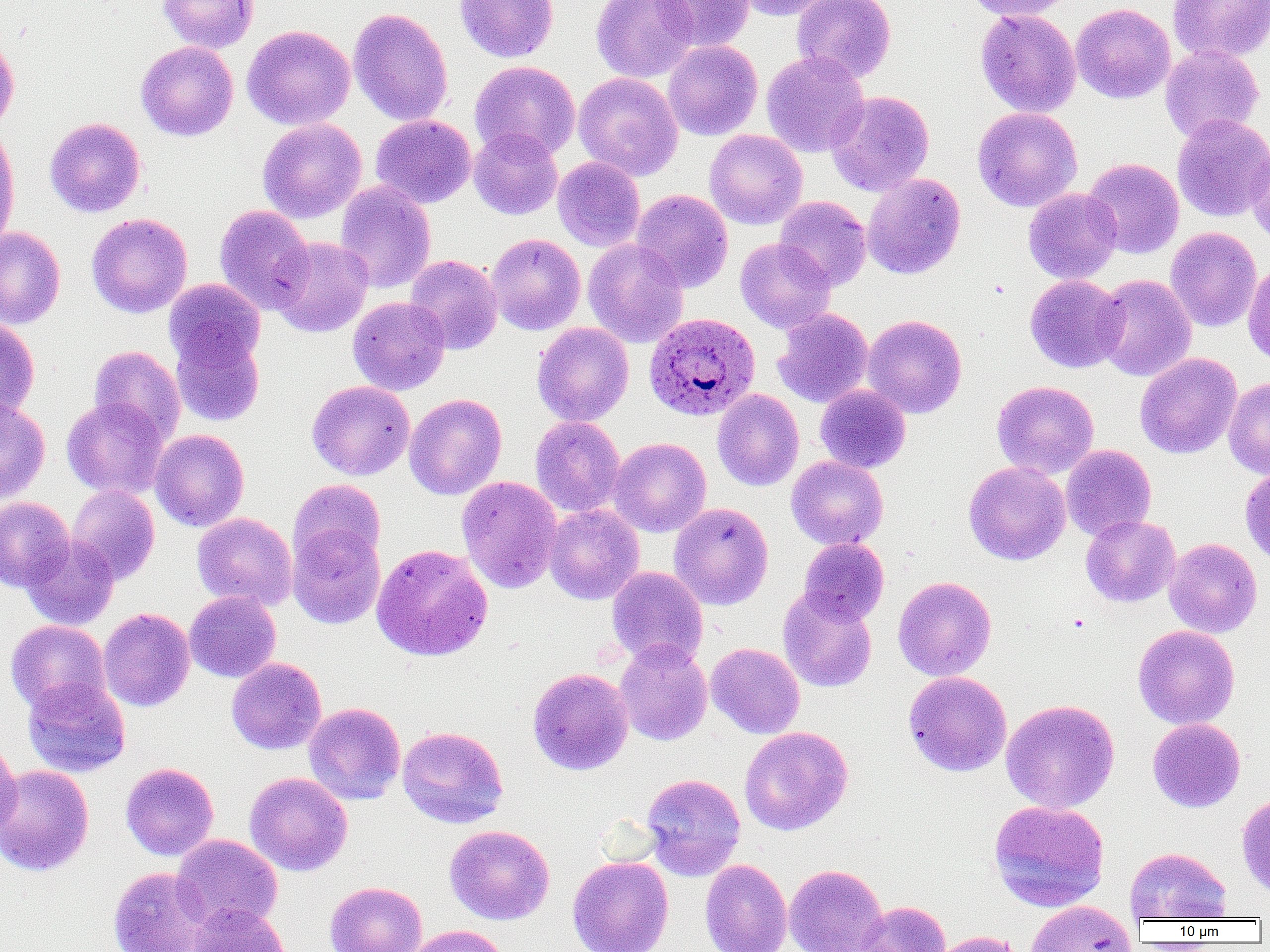

slide-level diagnosis = Plasmodium ovale
modality = optical microscopy
Plasmodium ovale-infected red blood cell locations = approximate bounding boxes as named x1/y1/x2/y2 corners in pixels: (x1=644, y1=312, x2=761, y2=422)
field of view = one of a larger specimen
image size = 1270×952 pixels
preparation = thin blood film
magnification = 1000x
uninfected red blood cell locations = approximate bounding boxes as named x1/y1/x2/y2 corners in pixels: (x1=156, y1=0, x2=259, y2=53), (x1=455, y1=0, x2=558, y2=63), (x1=591, y1=0, x2=699, y2=83), (x1=653, y1=0, x2=755, y2=51), (x1=733, y1=0, x2=839, y2=20), (x1=792, y1=0, x2=897, y2=84), (x1=963, y1=0, x2=1080, y2=21), (x1=1168, y1=0, x2=1270, y2=63), (x1=1071, y1=3, x2=1176, y2=104), (x1=348, y1=8, x2=453, y2=127), (x1=975, y1=8, x2=1081, y2=118), (x1=242, y1=24, x2=355, y2=130), (x1=0, y1=35, x2=19, y2=134), (x1=663, y1=39, x2=763, y2=140), (x1=136, y1=41, x2=238, y2=141), (x1=1160, y1=45, x2=1264, y2=141), (x1=761, y1=52, x2=869, y2=157), (x1=469, y1=61, x2=581, y2=160), (x1=574, y1=72, x2=683, y2=181), (x1=826, y1=91, x2=934, y2=196), (x1=973, y1=107, x2=1083, y2=212), (x1=1171, y1=114, x2=1270, y2=222), (x1=371, y1=115, x2=476, y2=208), (x1=44, y1=117, x2=146, y2=217), (x1=258, y1=118, x2=367, y2=223), (x1=0, y1=125, x2=19, y2=248), (x1=469, y1=128, x2=563, y2=220), (x1=704, y1=129, x2=807, y2=229), (x1=1246, y1=139, x2=1270, y2=247), (x1=553, y1=157, x2=645, y2=251), (x1=1083, y1=158, x2=1184, y2=259), (x1=862, y1=173, x2=966, y2=279), (x1=335, y1=181, x2=436, y2=293), (x1=1023, y1=188, x2=1122, y2=284), (x1=631, y1=189, x2=733, y2=293), (x1=775, y1=196, x2=872, y2=290), (x1=214, y1=204, x2=314, y2=315), (x1=86, y1=213, x2=193, y2=318), (x1=0, y1=226, x2=65, y2=329), (x1=1165, y1=227, x2=1263, y2=331), (x1=486, y1=234, x2=585, y2=335), (x1=269, y1=236, x2=373, y2=338), (x1=735, y1=237, x2=836, y2=334), (x1=583, y1=239, x2=688, y2=348), (x1=404, y1=254, x2=502, y2=354), (x1=1243, y1=258, x2=1270, y2=368), (x1=1025, y1=274, x2=1127, y2=373), (x1=1094, y1=274, x2=1196, y2=382), (x1=163, y1=279, x2=265, y2=372), (x1=348, y1=296, x2=450, y2=395), (x1=772, y1=308, x2=874, y2=407), (x1=862, y1=314, x2=966, y2=418), (x1=0, y1=319, x2=40, y2=421), (x1=532, y1=322, x2=634, y2=426), (x1=170, y1=325, x2=265, y2=427), (x1=89, y1=345, x2=185, y2=444), (x1=1135, y1=353, x2=1242, y2=459), (x1=1224, y1=378, x2=1270, y2=479), (x1=307, y1=380, x2=415, y2=480), (x1=992, y1=380, x2=1100, y2=479), (x1=815, y1=385, x2=911, y2=474), (x1=712, y1=389, x2=804, y2=491), (x1=405, y1=393, x2=506, y2=500), (x1=61, y1=397, x2=169, y2=499), (x1=0, y1=398, x2=50, y2=503), (x1=530, y1=416, x2=626, y2=518), (x1=150, y1=429, x2=249, y2=531), (x1=608, y1=437, x2=711, y2=537), (x1=1061, y1=444, x2=1156, y2=541), (x1=786, y1=456, x2=888, y2=550), (x1=963, y1=460, x2=1071, y2=565), (x1=1240, y1=466, x2=1270, y2=566), (x1=456, y1=476, x2=562, y2=593), (x1=288, y1=479, x2=386, y2=571), (x1=66, y1=485, x2=160, y2=584), (x1=0, y1=497, x2=75, y2=591), (x1=669, y1=502, x2=774, y2=610), (x1=543, y1=504, x2=644, y2=605), (x1=192, y1=512, x2=297, y2=611), (x1=1081, y1=515, x2=1180, y2=608), (x1=287, y1=523, x2=386, y2=629), (x1=21, y1=537, x2=120, y2=631), (x1=798, y1=538, x2=889, y2=625), (x1=1164, y1=538, x2=1262, y2=638), (x1=371, y1=543, x2=494, y2=662), (x1=606, y1=566, x2=708, y2=669), (x1=893, y1=576, x2=996, y2=680), (x1=778, y1=588, x2=877, y2=693), (x1=184, y1=591, x2=281, y2=682), (x1=98, y1=608, x2=195, y2=711), (x1=6, y1=620, x2=110, y2=715), (x1=1132, y1=625, x2=1239, y2=729), (x1=614, y1=639, x2=713, y2=746), (x1=706, y1=642, x2=805, y2=739), (x1=227, y1=658, x2=327, y2=754), (x1=527, y1=667, x2=634, y2=776), (x1=903, y1=671, x2=1012, y2=777), (x1=22, y1=677, x2=131, y2=777), (x1=1000, y1=699, x2=1120, y2=813), (x1=304, y1=702, x2=406, y2=805), (x1=1147, y1=717, x2=1246, y2=812), (x1=397, y1=726, x2=508, y2=828), (x1=739, y1=726, x2=853, y2=835), (x1=0, y1=739, x2=21, y2=842), (x1=120, y1=762, x2=219, y2=861), (x1=0, y1=764, x2=94, y2=876), (x1=244, y1=772, x2=353, y2=876), (x1=641, y1=773, x2=746, y2=880), (x1=1236, y1=792, x2=1270, y2=897), (x1=988, y1=799, x2=1110, y2=912), (x1=444, y1=825, x2=554, y2=924), (x1=171, y1=834, x2=283, y2=932), (x1=1125, y1=847, x2=1232, y2=922), (x1=567, y1=856, x2=674, y2=952), (x1=700, y1=859, x2=792, y2=952), (x1=784, y1=863, x2=887, y2=952), (x1=107, y1=866, x2=211, y2=952), (x1=326, y1=881, x2=427, y2=952), (x1=854, y1=900, x2=951, y2=952), (x1=1025, y1=901, x2=1137, y2=952), (x1=187, y1=903, x2=291, y2=952), (x1=404, y1=925, x2=509, y2=952), (x1=928, y1=931, x2=1026, y2=952)